Describe the morphology of the erythrocytes.
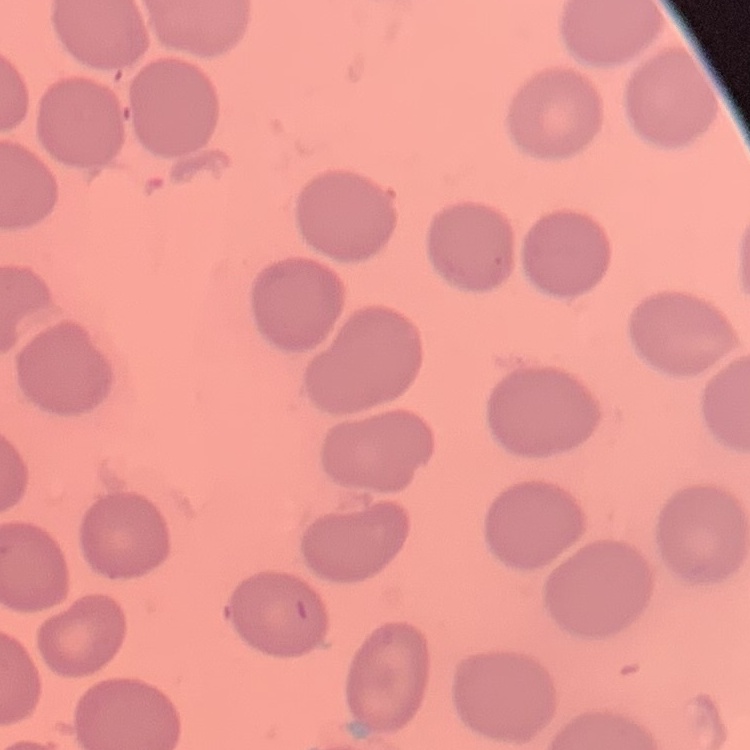

No rouleaux formation.

One tile cut from a larger photomicrograph. Thin blood smear. Stained with either Field's or Giemsa.